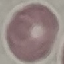
Summary:
  - Result: no malaria parasites seen
  - Capture: smartphone camera at the microscope eyepiece
  - Image type: automatically extracted cell patch, resized to 64 × 64 pixels
  - Preparation: thin blood smear
  - Stain: Giemsa